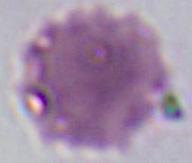
An erythrocyte is seen. 1000x magnification. Micrograph.